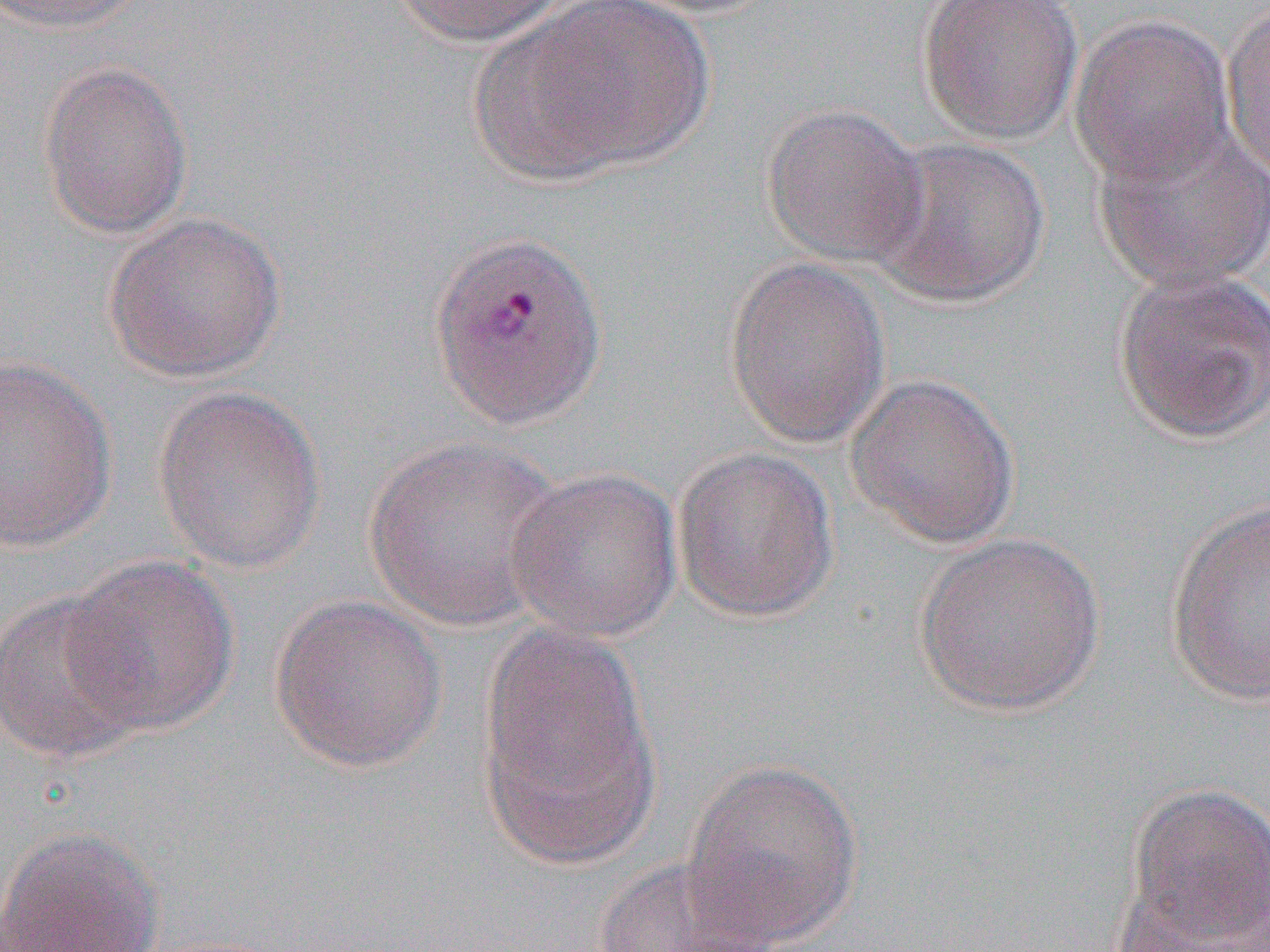
Approximate bounding boxes as (x1,y1)-(x2,y2) corner pairs in pixels. Uninfected red blood cell locations: (0,0)-(156,35), (385,0)-(571,47), (504,0)-(716,175), (916,0)-(1084,145), (1222,4)-(1270,182), (1069,15)-(1233,185), (38,60)-(193,239), (760,102)-(929,268), (1092,119)-(1270,294), (865,135)-(1052,309), (103,211)-(288,383), (723,257)-(891,448), (1112,266)-(1270,444), (0,354)-(117,552), (844,372)-(1021,550), (152,386)-(327,575), (361,436)-(570,633), (672,445)-(839,624), (505,467)-(683,642), (1164,497)-(1270,706), (912,532)-(1106,717), (61,554)-(240,736), (0,589)-(153,762), (269,594)-(448,772), (477,621)-(661,865), (679,757)-(866,947), (1122,783)-(1270,948), (0,824)-(166,952), (591,857)-(780,952), (1112,881)-(1270,951). Slide-level diagnosis: Plasmodium vivax. Single field of view. Image is 1270×952 pixels. 1000x magnification. Light microscopy. Thin blood film.